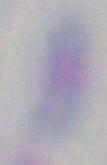
identification = Toxoplasma gondii
magnification = 1000x
modality = photomicrograph